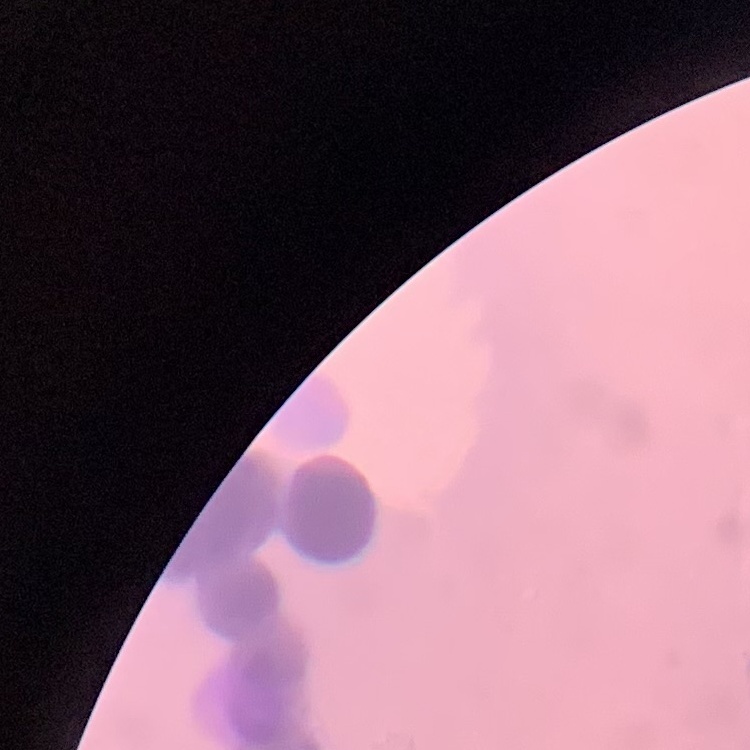
Summary:
  - Red blood cell morphology: rouleaux formation
  - Image type: square crop of a larger photomicrograph
  - Preparation: thin peripheral smear
  - Stain: Field's or Giemsa